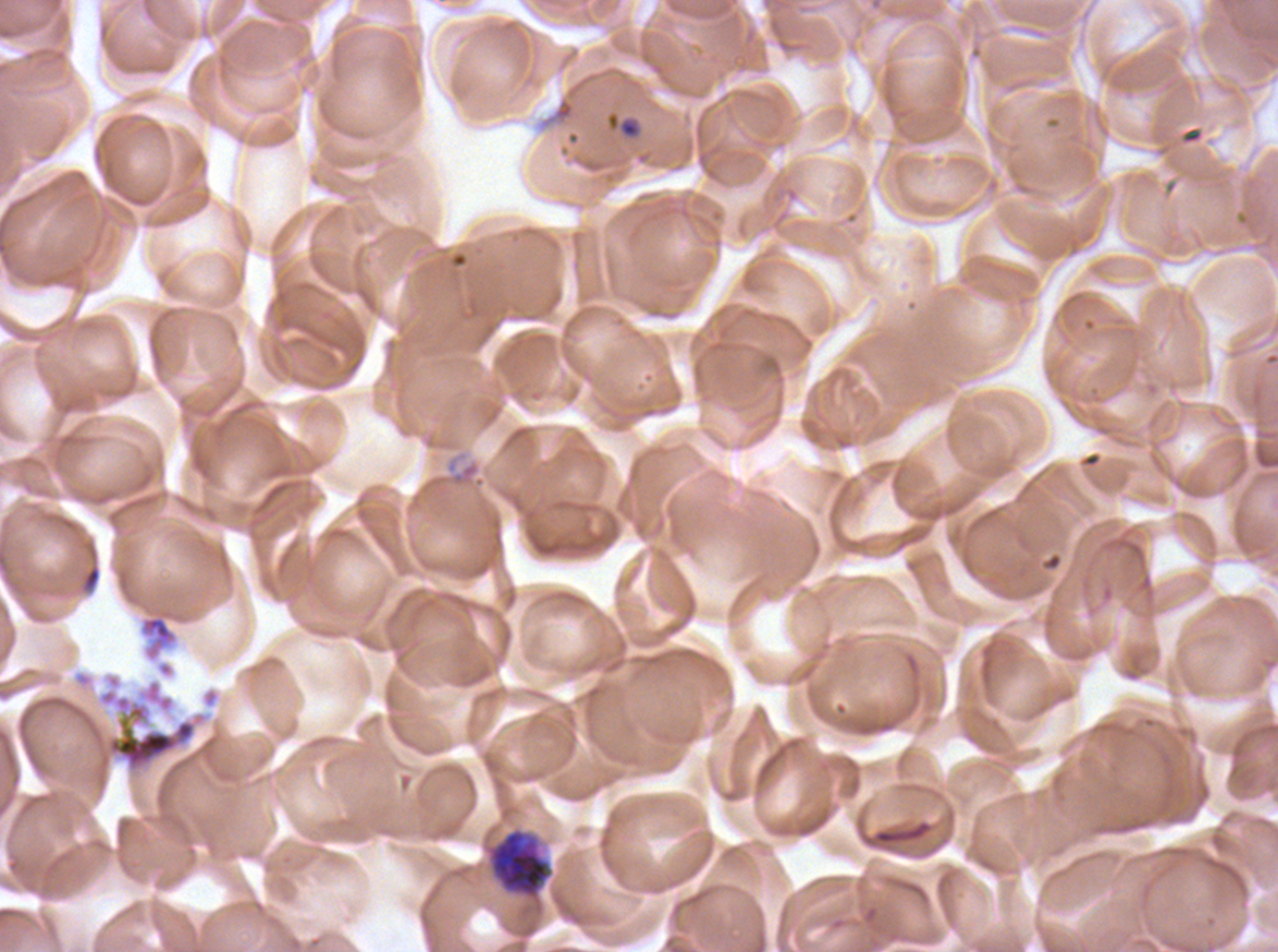
Approximate bounding boxes as (x1, y1, x2, y2) in pixels. Segmenter locations: (100, 689, 197, 772). Late schizont locations: (485, 826, 555, 904). Ring locations: (605, 110, 643, 140). Debris locations: (82, 566, 102, 591), (872, 819, 933, 846). Giemsa-stained preparation. Thin blood film. A sub-image separated from a larger composite. Life-cycle stages observed: ring, late schizont, segmenter. Plasmodium falciparum from a patient in The Gambia, cultured ex vivo for 24 to 48 hours. Image is 1278×952 pixels.